Classify this cell by malaria status.
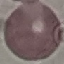

It is uninfected.

Summary:
  - Image type: cell patch, automatically extracted from a larger field of view and resized to 64 × 64 pixels
  - Stain: Giemsa
  - Preparation: thin smear
  - Capture: smartphone through the microscope eyepiece